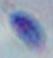
{
  "identification": "Toxoplasma gondii",
  "modality": "photomicrograph",
  "magnification": "1000x"
}